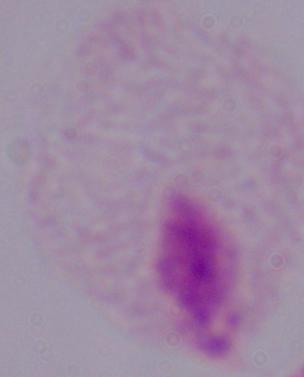
Summary:
  - Modality: photomicrograph
  - Identification: trichomonad
  - Magnification: 1000x